State the blood parasite species.
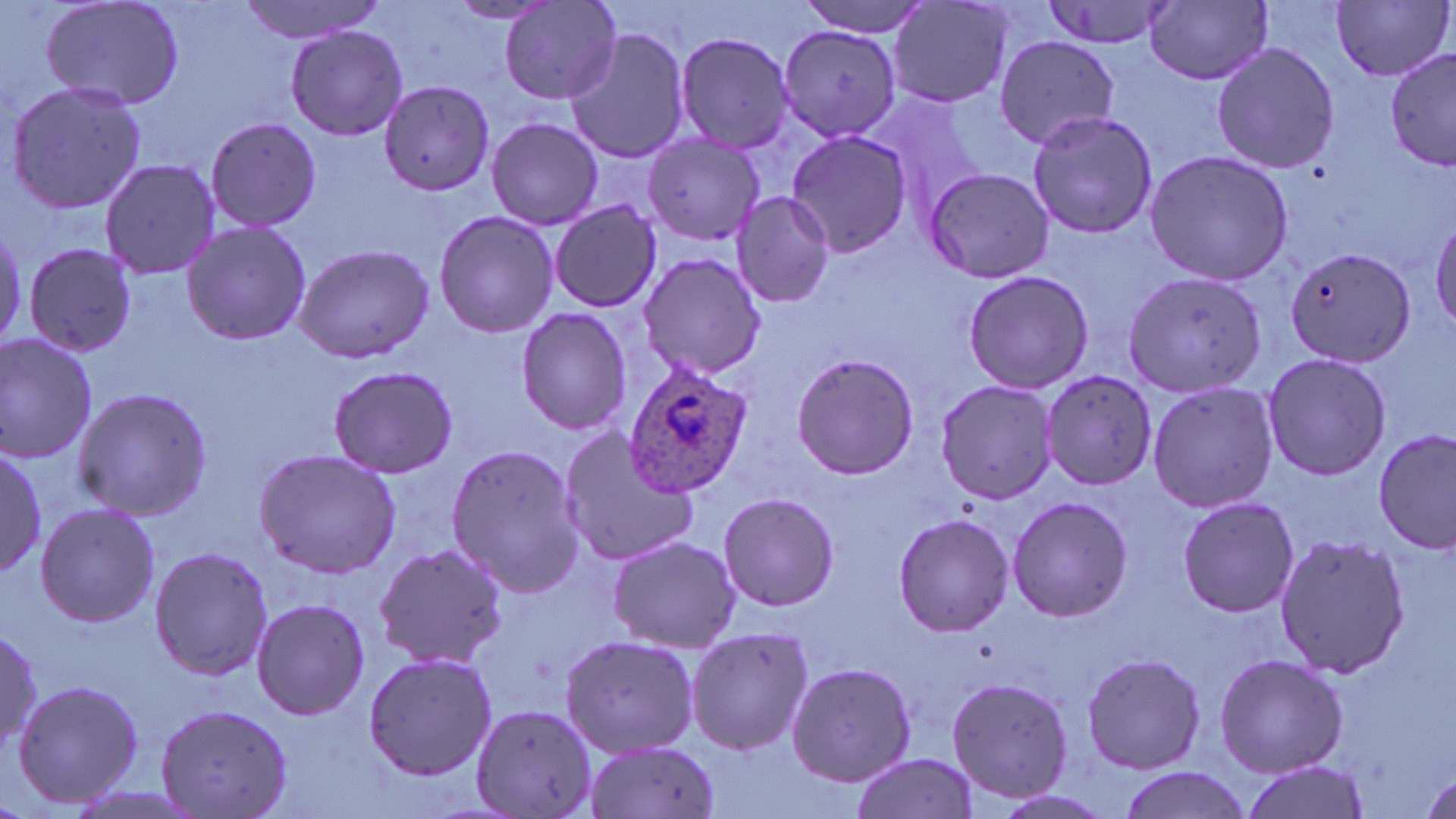

Plasmodium ovale.

Summary:
  - Coordinate format: approximate bounding boxes as named x1/y1/x2/y2 corners in pixels
  - Plasmodium ovale-infected red blood cell locations: (x1=620, y1=358, x2=755, y2=498)
  - Uninfected red blood cell locations: (x1=38, y1=0, x2=186, y2=112), (x1=238, y1=0, x2=388, y2=42), (x1=794, y1=0, x2=932, y2=37), (x1=1038, y1=0, x2=1177, y2=51), (x1=1331, y1=0, x2=1453, y2=82), (x1=501, y1=1, x2=623, y2=106), (x1=887, y1=1, x2=1018, y2=111), (x1=444, y1=2, x2=560, y2=26), (x1=1146, y1=2, x2=1274, y2=86), (x1=285, y1=25, x2=407, y2=141), (x1=563, y1=25, x2=692, y2=165), (x1=777, y1=25, x2=901, y2=141), (x1=672, y1=30, x2=798, y2=155), (x1=993, y1=37, x2=1120, y2=149), (x1=1210, y1=40, x2=1340, y2=175), (x1=1385, y1=48, x2=1456, y2=173), (x1=4, y1=80, x2=150, y2=216), (x1=377, y1=80, x2=495, y2=199), (x1=863, y1=91, x2=995, y2=222), (x1=1024, y1=109, x2=1160, y2=240), (x1=487, y1=116, x2=605, y2=230), (x1=202, y1=117, x2=323, y2=233), (x1=785, y1=131, x2=914, y2=258), (x1=642, y1=132, x2=767, y2=245), (x1=1142, y1=150, x2=1294, y2=285), (x1=99, y1=158, x2=222, y2=280), (x1=923, y1=169, x2=1055, y2=282), (x1=730, y1=192, x2=835, y2=309), (x1=548, y1=201, x2=661, y2=313), (x1=432, y1=209, x2=558, y2=339), (x1=1429, y1=213, x2=1456, y2=332), (x1=180, y1=221, x2=311, y2=346), (x1=21, y1=241, x2=139, y2=353), (x1=289, y1=243, x2=436, y2=364), (x1=1282, y1=246, x2=1418, y2=368), (x1=639, y1=251, x2=770, y2=382), (x1=1121, y1=263, x2=1267, y2=395), (x1=961, y1=270, x2=1094, y2=394), (x1=515, y1=308, x2=632, y2=434), (x1=0, y1=331, x2=100, y2=463), (x1=1261, y1=351, x2=1392, y2=481), (x1=790, y1=352, x2=919, y2=480), (x1=326, y1=363, x2=460, y2=480), (x1=1040, y1=371, x2=1159, y2=492), (x1=935, y1=380, x2=1060, y2=504), (x1=1146, y1=381, x2=1281, y2=515), (x1=70, y1=386, x2=212, y2=520), (x1=555, y1=425, x2=701, y2=567), (x1=1375, y1=430, x2=1454, y2=556), (x1=444, y1=441, x2=586, y2=598), (x1=0, y1=447, x2=46, y2=578), (x1=252, y1=449, x2=403, y2=578), (x1=718, y1=492, x2=839, y2=610), (x1=1177, y1=495, x2=1300, y2=618), (x1=1007, y1=497, x2=1133, y2=621), (x1=34, y1=502, x2=159, y2=628), (x1=891, y1=513, x2=1015, y2=638), (x1=1273, y1=531, x2=1410, y2=681), (x1=605, y1=535, x2=739, y2=652), (x1=373, y1=542, x2=510, y2=669), (x1=148, y1=545, x2=273, y2=682), (x1=250, y1=597, x2=371, y2=719), (x1=0, y1=624, x2=44, y2=754), (x1=685, y1=626, x2=814, y2=756), (x1=559, y1=633, x2=699, y2=757), (x1=361, y1=649, x2=495, y2=781), (x1=1080, y1=650, x2=1207, y2=774), (x1=1213, y1=653, x2=1348, y2=777), (x1=786, y1=661, x2=916, y2=788), (x1=946, y1=677, x2=1073, y2=801), (x1=10, y1=679, x2=145, y2=810), (x1=153, y1=703, x2=294, y2=819), (x1=470, y1=703, x2=599, y2=819), (x1=582, y1=738, x2=722, y2=819), (x1=850, y1=754, x2=980, y2=819), (x1=1237, y1=761, x2=1369, y2=819), (x1=1115, y1=766, x2=1251, y2=819)
  - Modality: light microscopy
  - Field of view: one of a larger specimen
  - Preparation: thin blood film
  - Image size: 1456×819 pixels
  - Stain: May-Grünwald-Giemsa
  - Magnification: 1000x